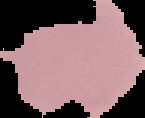

Summary:
  - Image size: 145×118 pixels
  - Preparation: thin blood smear
  - Image type: segmented cell region on a black background
  - Malaria status: uninfected